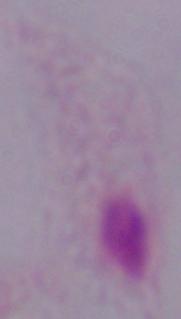
A trichomonad is seen. Micrograph. Captured at 1000x magnification.